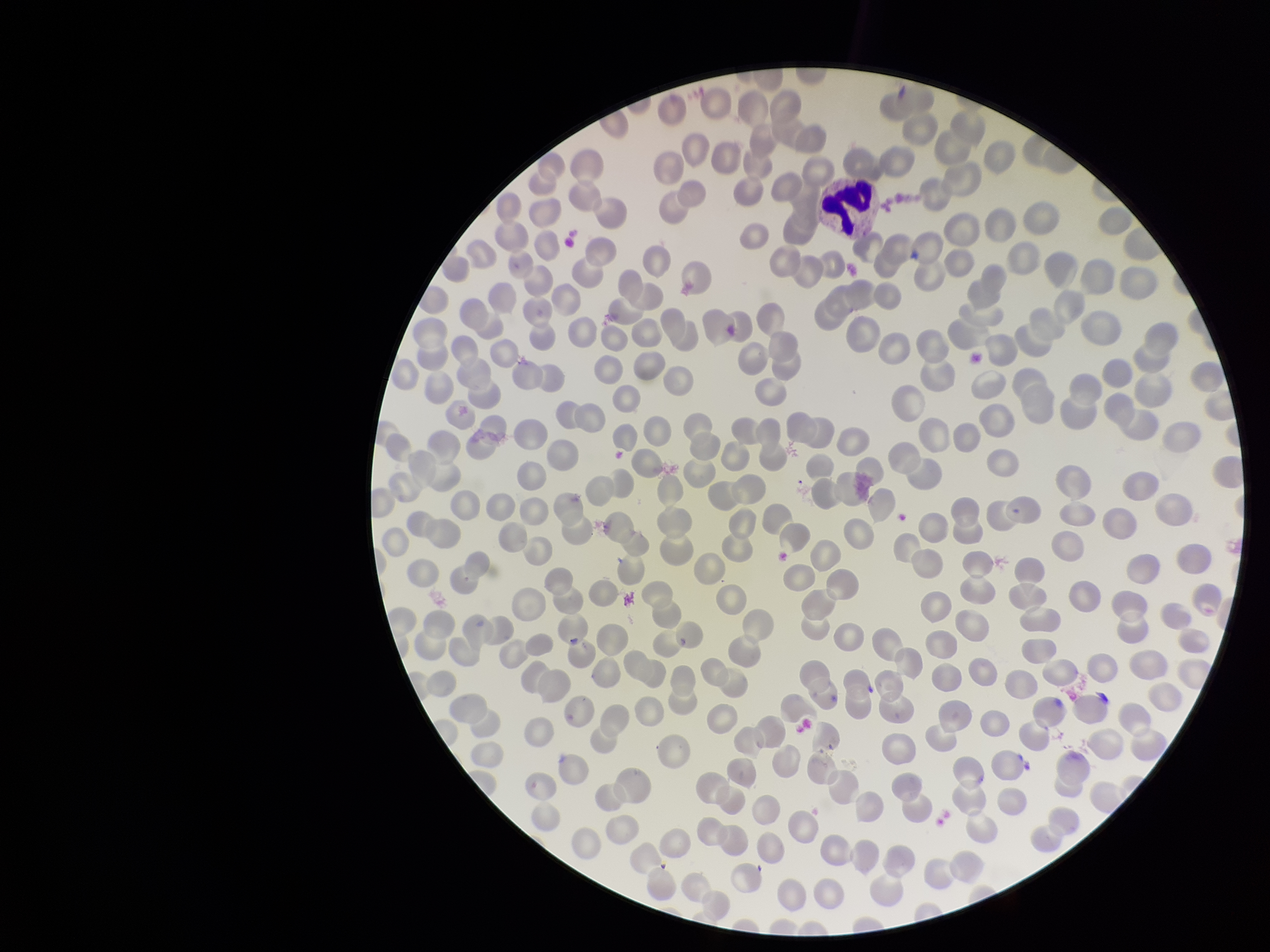

Parasitized red blood cell count: 0. Single field of view. Parasitized red blood cells: none detected. Patient malaria status: negative. Photographed through the microscope eyepiece with a smartphone camera. Stained with Giemsa. Preparation: thin blood smear. Image is 1270×952 pixels. Red blood cell count: 290.